Assess for Plasmodium parasites.
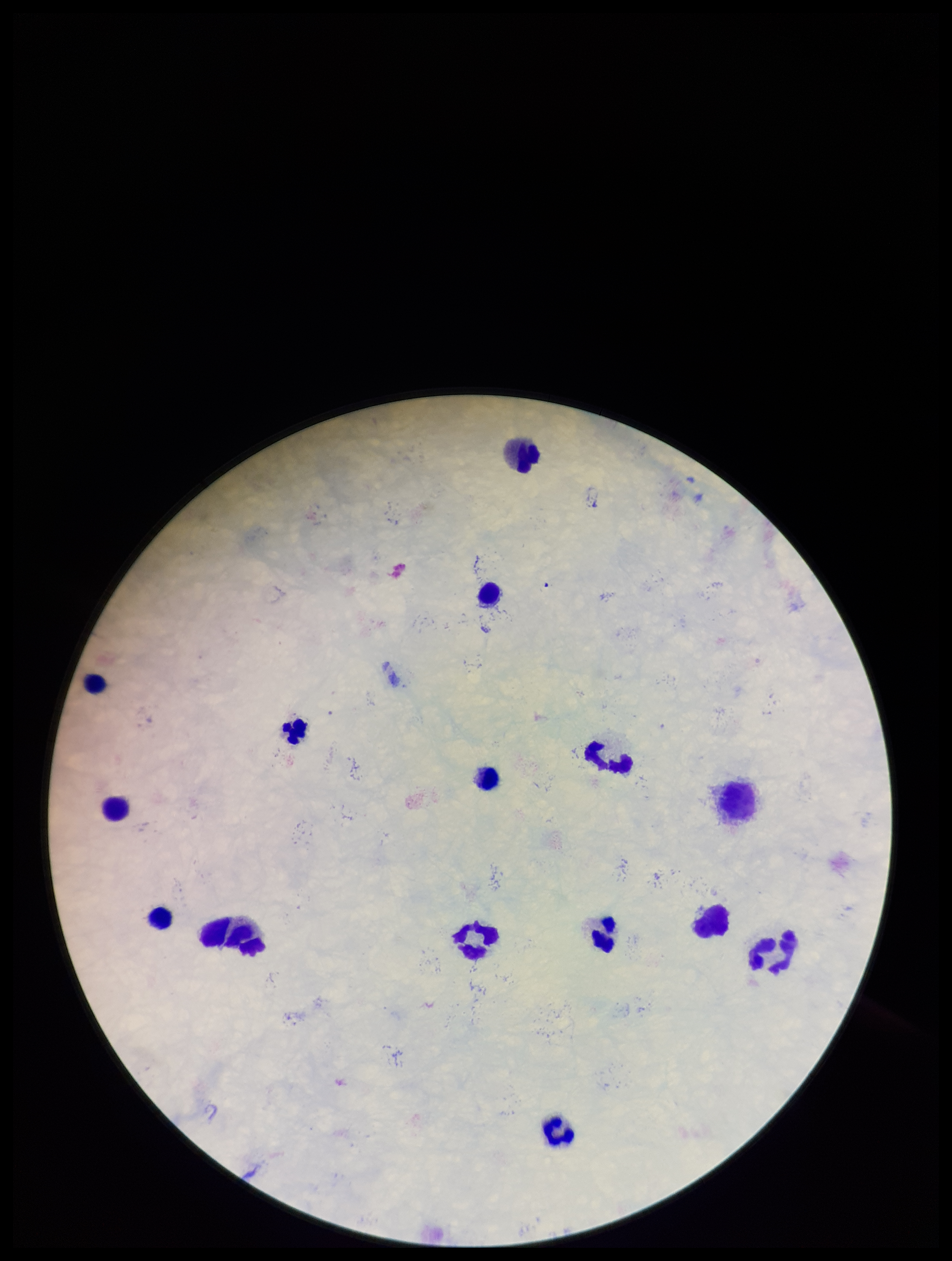
None detected.

Summary:
  - Stain: Giemsa
  - Field of view: single
  - Patient malaria status: negative
  - Image size: 952×1261 pixels
  - Preparation: thick smear
  - Capture: smartphone photograph through the microscope eyepiece
  - Parasite count: 0
  - Leukocyte count: 14